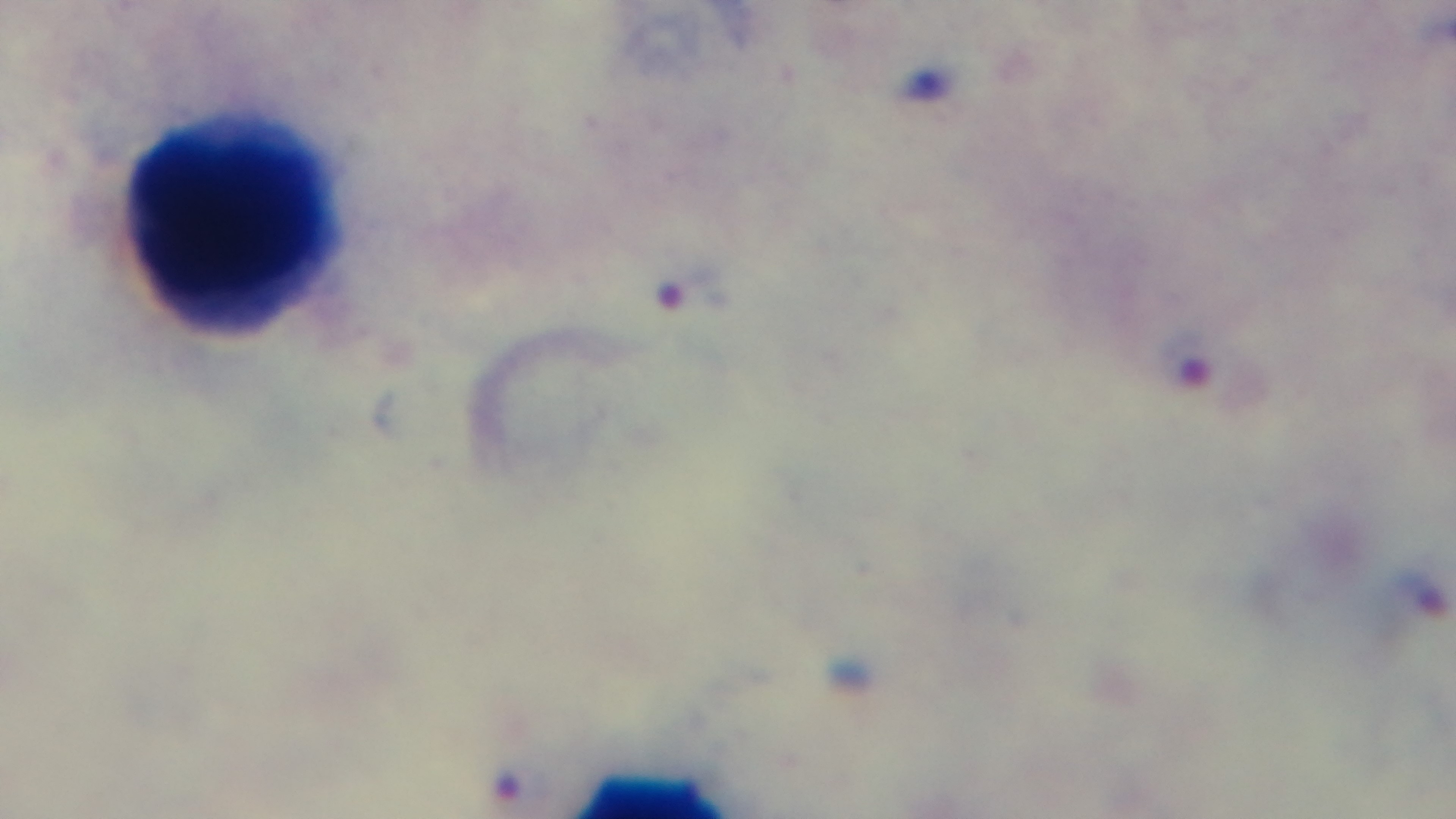

stain = Giemsa
field of view = one from the slide
modality = light microscopy
preparation = thick smear
objective = 100x oil immersion
malaria status = positive
capture = mounted 4K digital camera